State which cell type is depicted.
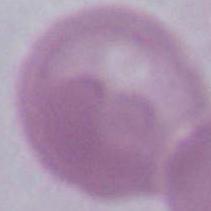

This is an erythrocyte.

1000x magnification. Micrograph.